Give the position of every leukocyte visible.
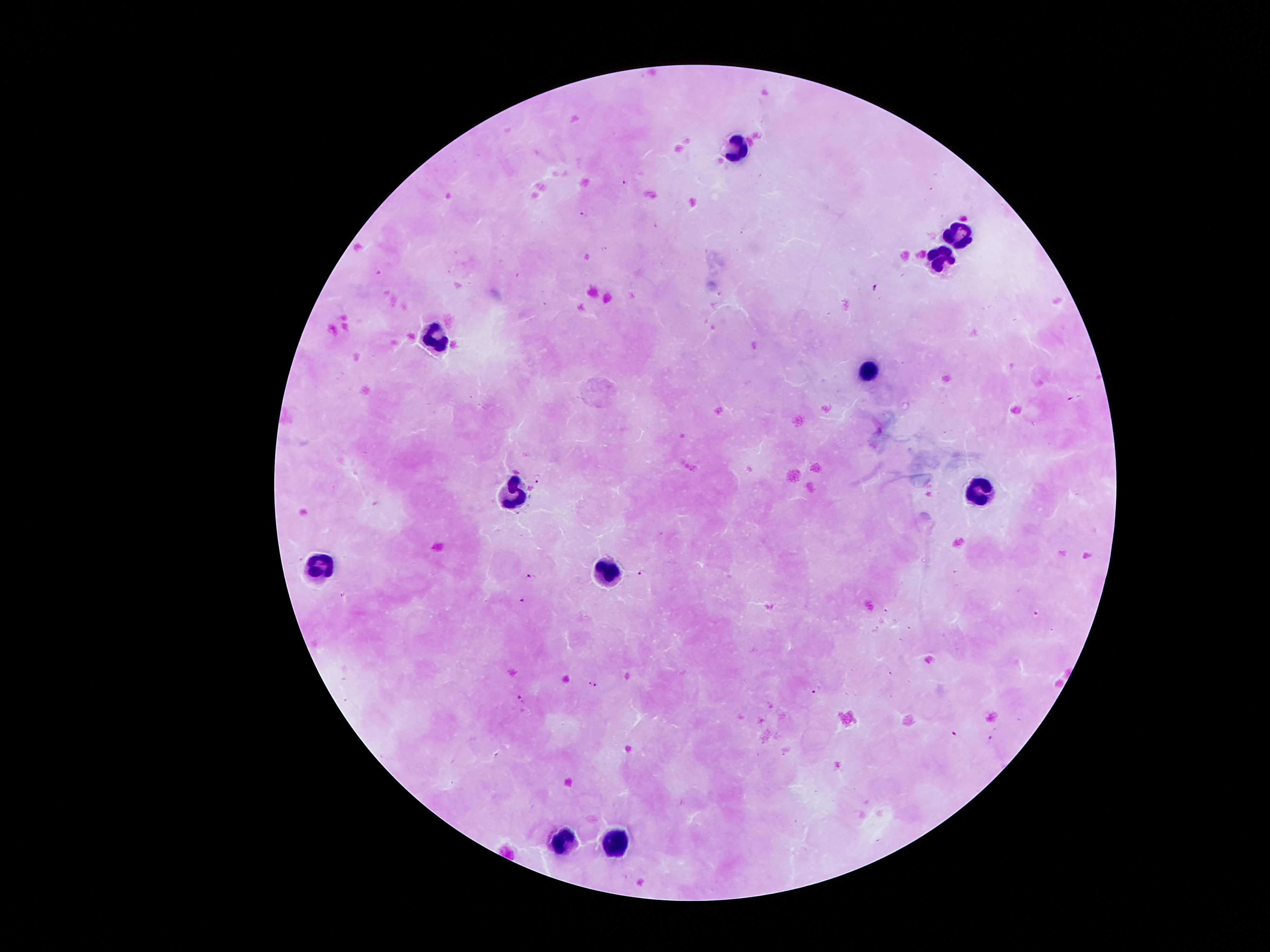

Approximate object centers, in pixels from the top-left corner.
Leukocytes: (x=730, y=149), (x=957, y=235), (x=940, y=257), (x=439, y=336), (x=869, y=368), (x=506, y=490), (x=978, y=494), (x=320, y=564), (x=603, y=571), (x=555, y=844), (x=620, y=844).

Plasmodium parasite locations: (x=624, y=183), (x=586, y=214), (x=537, y=478), (x=516, y=514), (x=642, y=573), (x=531, y=576), (x=520, y=599), (x=589, y=684), (x=596, y=685), (x=812, y=692), (x=520, y=696), (x=954, y=735), (x=992, y=738). Patient malaria status: infected with Plasmodium falciparum. Thick blood smear. Smartphone photograph taken through the microscope eyepiece. Giemsa stain. Single field of view. Image is 1270×952 pixels. 100x magnification.